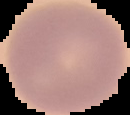

Malaria status: uninfected. From a thin blood smear. Cell region segmented out of the field of view; the surrounding area is masked to black. Image is 130×115 pixels.